Name the cell type shown.
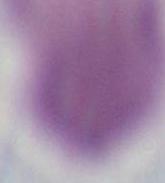
This is an erythrocyte.

modality = micrograph
magnification = 1000x